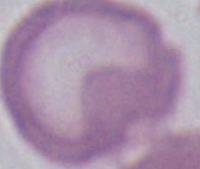 Micrograph. An erythrocyte is shown. Captured at 1000x magnification.